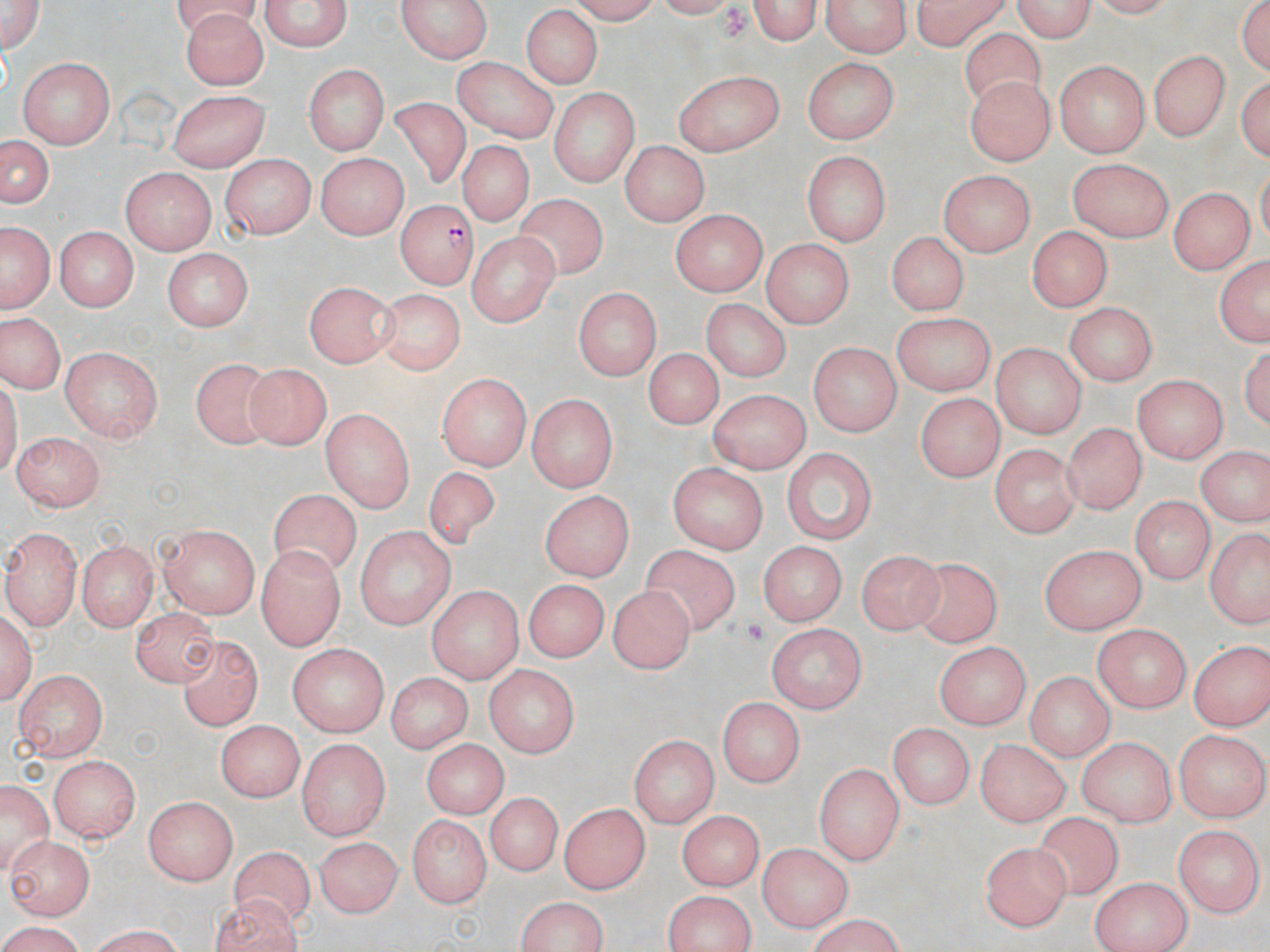

Summary:
  - Coordinate format: approximate bounding boxes as (x1,y1)-(x2,y2) corner pairs in pixels
  - Plasmodium falciparum-infected red blood cell locations: (393,198)-(473,288)
  - Uninfected red blood cell locations: (256,0)-(353,53), (744,0)-(825,44), (819,0)-(911,58), (908,0)-(1010,49), (1004,0)-(1099,40), (1236,0)-(1270,78), (0,1)-(46,53), (396,1)-(497,62), (518,6)-(607,88), (181,9)-(271,86), (962,30)-(1048,115), (1152,49)-(1229,137), (801,56)-(897,142), (15,57)-(116,148), (455,59)-(562,145), (1053,60)-(1150,156), (304,64)-(387,159), (674,68)-(783,157), (1236,71)-(1267,171), (964,75)-(1053,167), (549,88)-(638,186), (173,90)-(272,172), (387,96)-(479,190), (0,133)-(54,213), (621,140)-(710,227), (457,141)-(533,229), (803,151)-(890,246), (316,154)-(405,239), (222,157)-(313,237), (1070,159)-(1172,238), (118,167)-(214,255), (939,170)-(1037,256), (1169,186)-(1250,274), (516,195)-(608,275), (670,209)-(770,292), (2,223)-(52,313), (57,224)-(140,310), (1024,225)-(1115,310), (469,231)-(557,331), (885,231)-(968,316), (764,240)-(854,326), (160,250)-(251,333), (1212,255)-(1270,349), (304,281)-(398,365), (379,289)-(464,372), (573,289)-(659,380), (697,299)-(789,385), (1064,302)-(1158,385), (891,312)-(995,396), (0,313)-(66,391), (808,340)-(900,438), (993,340)-(1086,438), (62,347)-(164,443), (649,347)-(718,431), (191,353)-(277,451), (243,361)-(332,451), (437,374)-(528,470), (1132,375)-(1225,461), (707,387)-(815,469), (917,390)-(1003,479), (526,393)-(618,493), (321,409)-(414,511), (1061,418)-(1145,513), (12,430)-(101,512), (991,442)-(1079,538), (783,446)-(879,543), (1197,446)-(1266,527), (426,462)-(499,554), (669,462)-(771,552), (270,490)-(363,585), (539,490)-(636,582), (1132,496)-(1211,582), (161,523)-(260,617), (355,524)-(458,629), (6,526)-(79,631), (1203,526)-(1270,632), (75,539)-(159,630), (760,540)-(844,627), (1038,543)-(1148,636), (640,545)-(738,636), (856,547)-(946,637), (259,548)-(344,648), (910,555)-(1002,646), (521,579)-(613,661), (426,585)-(527,683), (609,586)-(698,675), (134,606)-(219,686), (1,607)-(38,709), (766,622)-(870,709), (1094,625)-(1190,711), (181,635)-(259,732), (1188,639)-(1269,729), (935,642)-(1029,729), (286,644)-(390,735), (487,662)-(578,759), (15,669)-(109,760), (1023,670)-(1114,759), (388,671)-(470,756), (717,696)-(803,786), (215,721)-(308,800), (890,724)-(972,811), (1176,732)-(1267,822), (628,734)-(716,826), (1076,736)-(1177,826), (975,737)-(1068,826), (298,738)-(390,841), (422,738)-(510,816), (48,757)-(141,845), (816,764)-(903,864), (0,777)-(53,876), (491,791)-(558,877), (145,797)-(239,886), (559,801)-(650,895), (676,809)-(764,891), (406,814)-(492,907), (1039,815)-(1123,901), (1169,823)-(1262,913), (7,833)-(95,917), (313,838)-(402,919), (759,841)-(854,931), (981,841)-(1068,929), (229,847)-(313,928), (1090,876)-(1192,951), (207,890)-(301,948), (661,892)-(758,952), (513,894)-(611,952), (795,918)-(914,951), (0,920)-(94,950), (76,924)-(191,952)
  - Platelet locations: (742,615)-(771,649)
  - Slide-level diagnosis: Plasmodium falciparum
  - Stain: May-Grünwald-Giemsa
  - Modality: light microscopy
  - Magnification: 1000x
  - Field of view: one of a larger specimen
  - Image size: 1270×952 pixels
  - Preparation: thin blood film